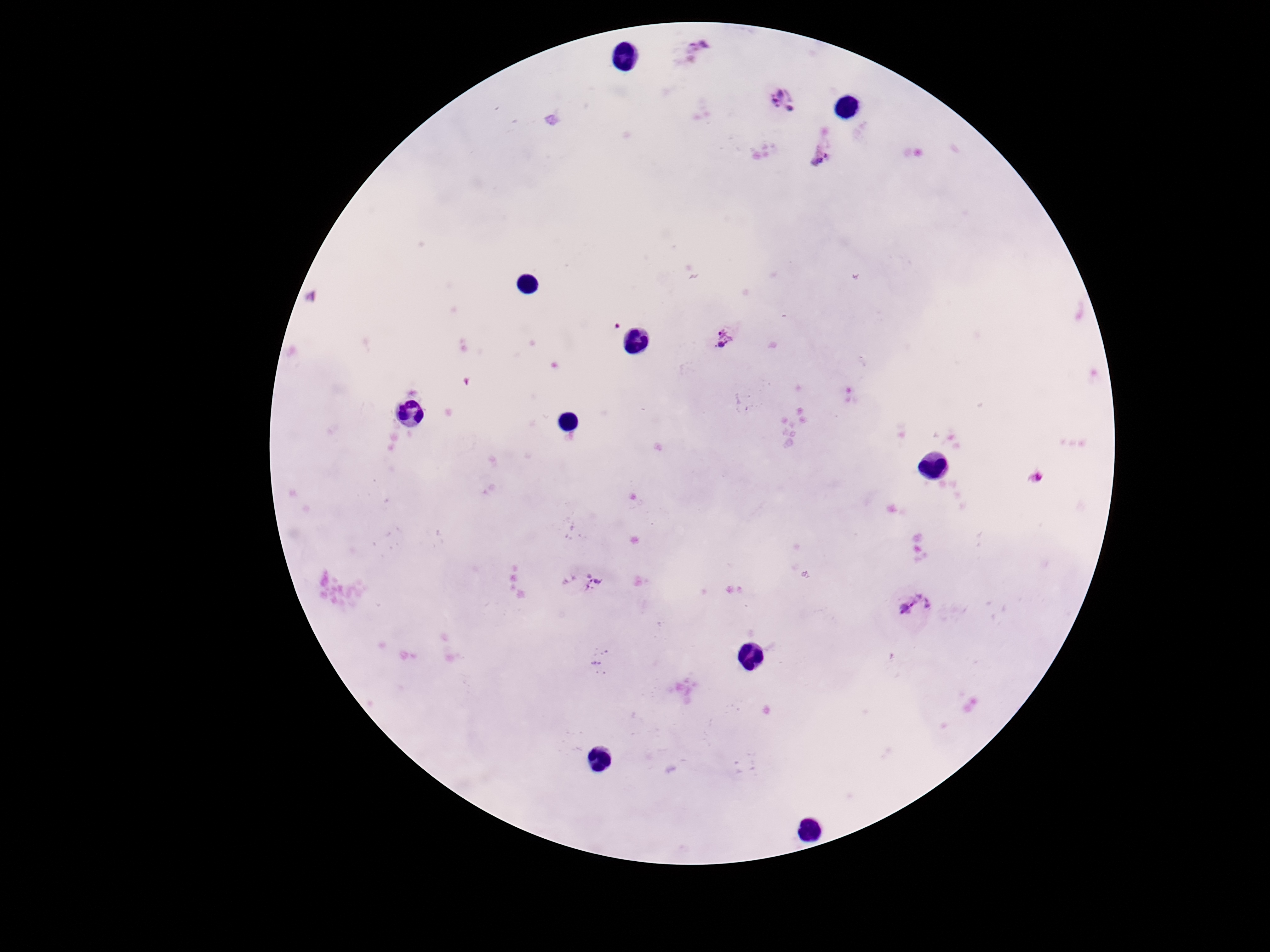

Approximate centers as {x, y} in pixels.
Summary:
  - Plasmodium parasite locations: {696, 50}, {786, 98}, {823, 150}, {310, 297}, {724, 339}, {1036, 478}, {592, 583}, {916, 602}
  - Magnification: 100x
  - Capture: smartphone camera through the microscope eyepiece
  - Preparation: thick blood film
  - Field of view: single
  - Patient malaria status: infected
  - Image size: 1270×952 pixels
  - Stain: Giemsa